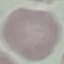

Result: no malaria parasites detected. Thin blood smear. Cell patch, automatically extracted from a larger field of view and resized to 64 × 64 pixels. Giemsa stain. Acquired by smartphone through the microscope eyepiece.